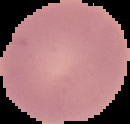

Summary:
  - Malaria status: uninfected
  - Preparation: thin blood smear
  - Image type: segmented cell region on a black background
  - Image size: 130×124 pixels